Outline each blood parasite and name the species.
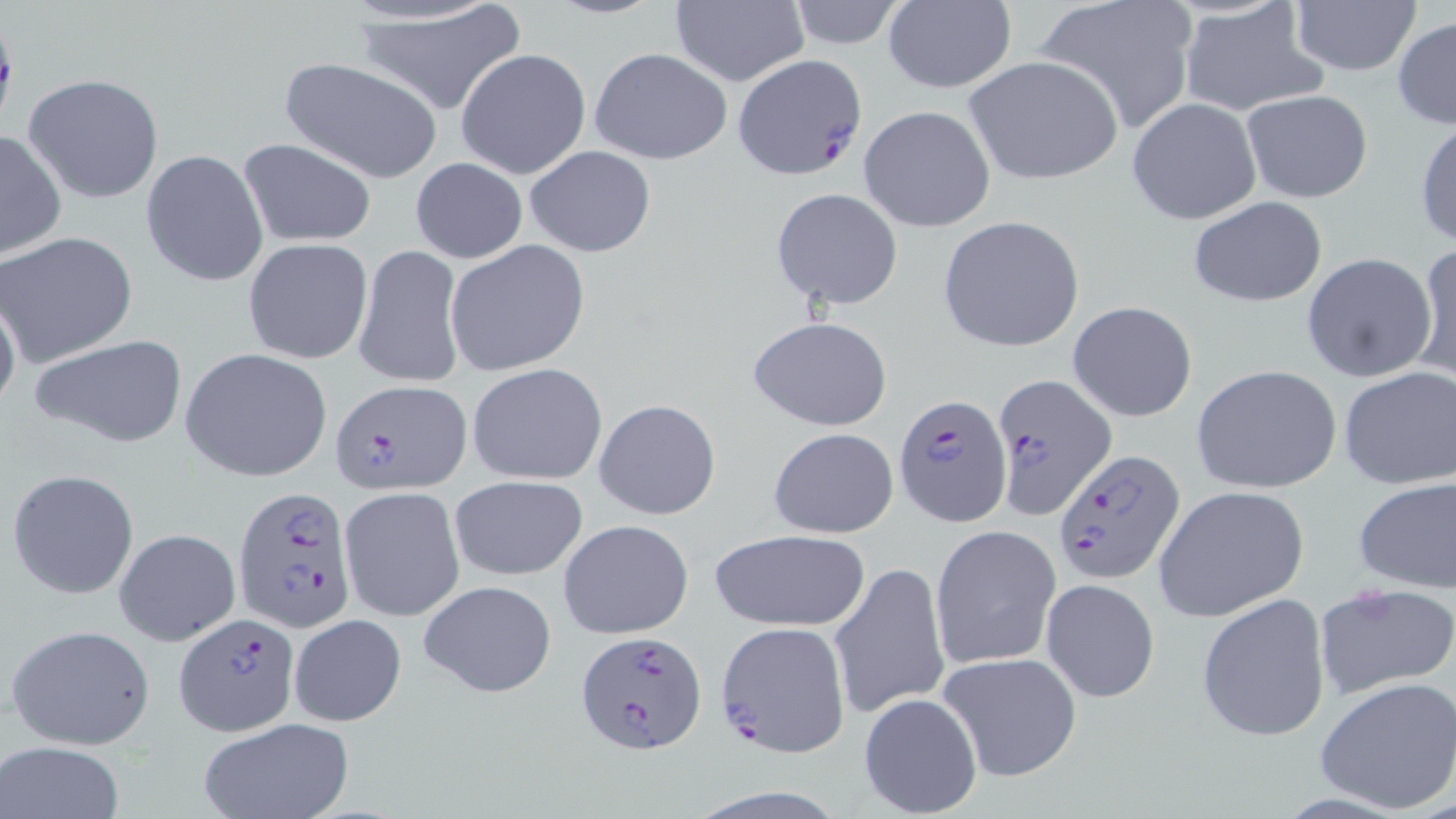
Approximate bounding boxes as (x1,y1)-(x2,y2) corner pairs in pixels.
Plasmodium falciparum-infected red blood cells: (732,53)-(866,180), (991,371)-(1116,520), (328,379)-(470,495), (893,394)-(1014,528), (1052,448)-(1184,586), (233,486)-(359,633), (174,613)-(298,736), (716,620)-(851,756), (573,629)-(707,754).
No Plasmodium ovale, Plasmodium malariae, Plasmodium vivax, Babesia divergens, or Trypanosoma brucei observed.

Uninfected red blood cell locations: (1031,0)-(1201,134), (351,1)-(525,117), (668,1)-(808,87), (784,1)-(910,50), (882,1)-(1016,94), (1289,1)-(1421,78), (1175,4)-(1328,118), (1392,17)-(1456,127), (590,47)-(732,164), (455,48)-(591,179), (962,55)-(1124,185), (278,57)-(444,184), (24,73)-(165,204), (1240,91)-(1373,204), (1127,98)-(1262,225), (859,105)-(996,233), (1414,117)-(1456,251), (0,129)-(66,260), (238,138)-(377,246), (524,145)-(656,258), (141,148)-(270,287), (411,158)-(526,264), (771,187)-(903,311), (1185,197)-(1329,307), (937,216)-(1085,354), (1,232)-(139,366), (243,237)-(373,363), (444,239)-(590,377), (353,243)-(466,391), (1412,243)-(1456,387), (1301,252)-(1438,383), (0,287)-(21,419), (1067,301)-(1198,422), (747,316)-(893,430), (30,333)-(190,449), (181,348)-(333,482), (467,363)-(608,486), (1190,364)-(1342,494), (1338,366)-(1456,491), (593,398)-(721,521), (768,428)-(899,538), (7,469)-(140,599), (448,474)-(589,582), (1352,475)-(1456,596), (1153,485)-(1310,625), (340,487)-(464,621), (560,520)-(691,637), (930,524)-(1061,672), (114,528)-(240,646), (708,530)-(871,634), (829,561)-(950,721), (1041,578)-(1159,704), (418,580)-(556,698), (1313,580)-(1456,701), (1195,592)-(1332,743), (288,613)-(407,727), (6,623)-(155,750), (938,651)-(1080,780), (1315,677)-(1456,815), (858,693)-(983,817), (196,719)-(356,819), (2,741)-(126,819). Slide-level diagnosis: Plasmodium falciparum. Captured at 1000x magnification. Light microscopy. Image is 1456×819 pixels. Thin blood film. One field of a larger specimen. May-Grünwald-Giemsa stain.